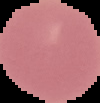

preparation = thin blood smear
image size = 100×103 pixels
malaria status = uninfected
image type = segmented cell region on a black background